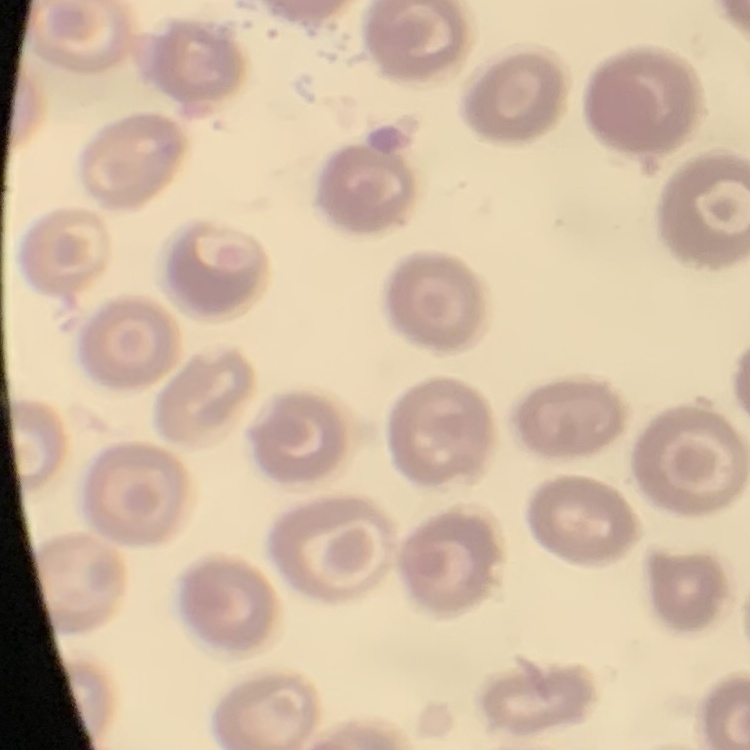
The red blood cells show no rouleaux formation. Field's or Giemsa stain. Thin blood smear. One tile cut from a larger photomicrograph.